Classify this cell by malaria status.
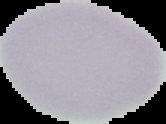

Uninfected.

Segmented cell region on a black background. From a thin blood film. Image is 166×124 pixels.